Describe the morphology of the red blood cells.
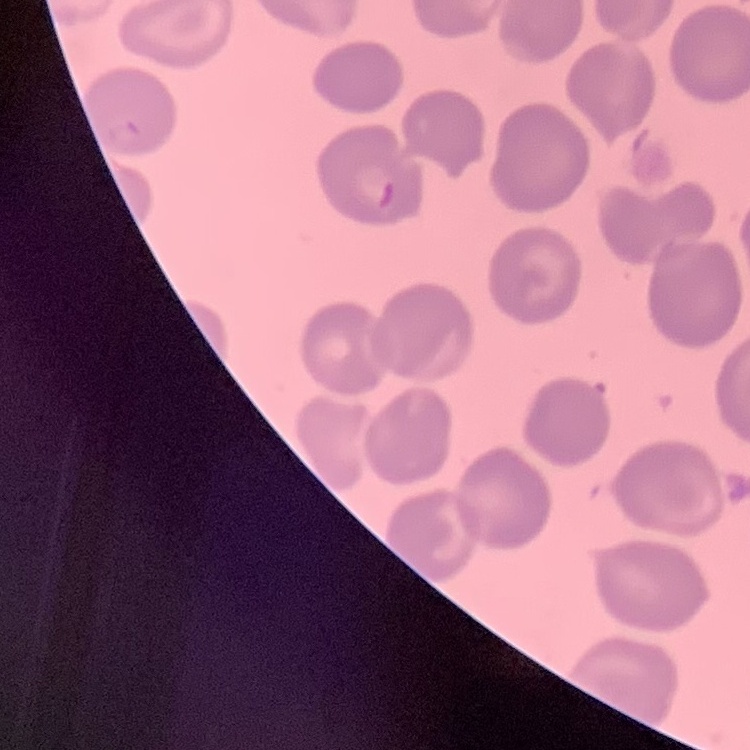
No rouleaux formation.

preparation = thin blood smear
stain = Field's or Giemsa
image type = one tile cut from a larger photomicrograph